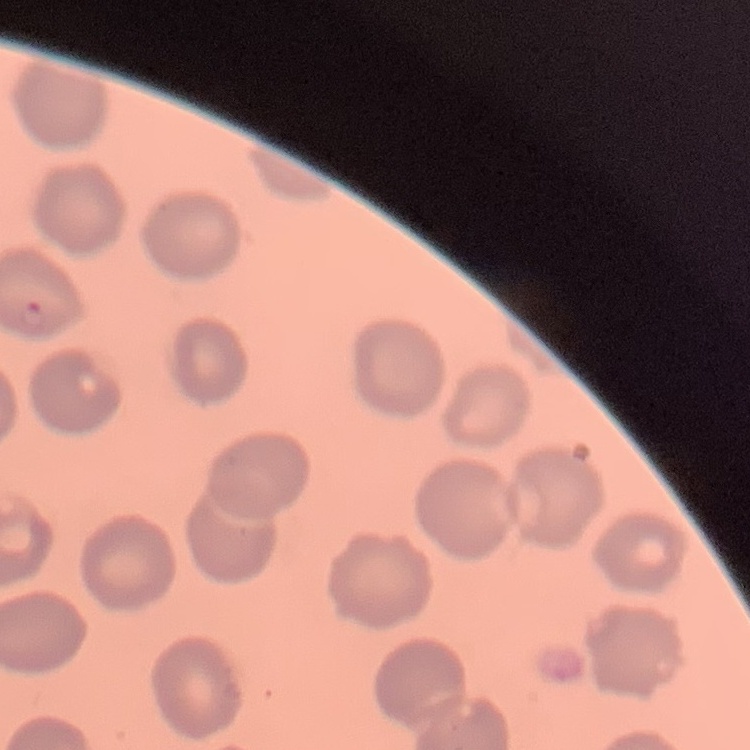
Summary:
  - Erythrocyte morphology: no rouleaux formation
  - Image type: one tile cut from a larger photomicrograph
  - Preparation: thin peripheral smear
  - Stain: Field's or Giemsa